Assess this cell for malaria.
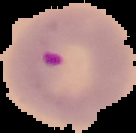
Parasitized.

Summary:
  - Image size: 136×133 pixels
  - Preparation: thin blood smear
  - Image type: segmented cell region on a black background